Assess this cell for malaria.
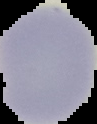

Uninfected.

Summary:
  - Image type: segmented cell region on a black background
  - Image size: 97×124 pixels
  - Preparation: thin blood smear